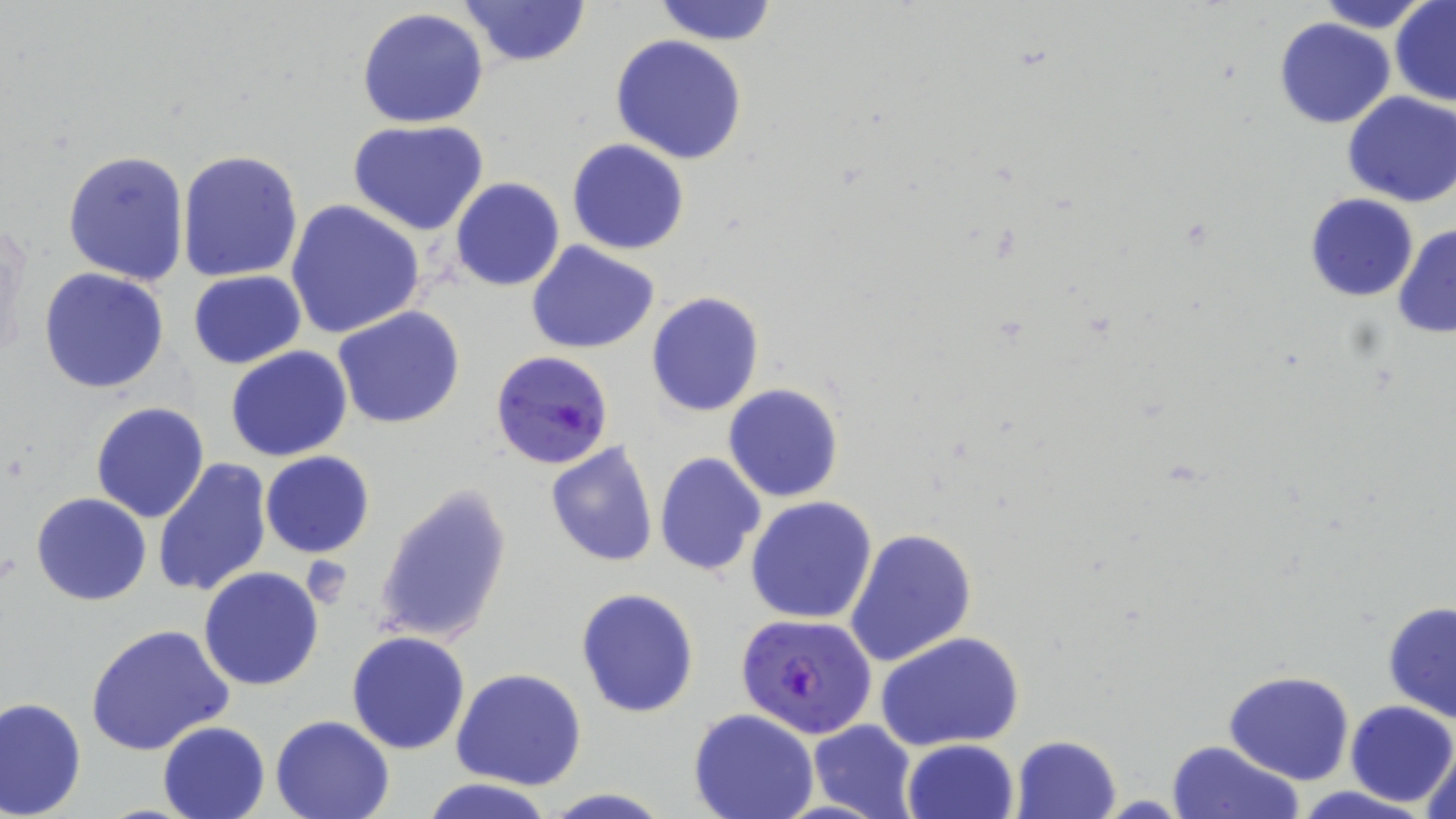
Summary:
  - Coordinate format: approximate bounding boxes as (x1,y1)-(x2,y2) corner pairs in pixels
  - Uninfected red blood cell locations: (456,0)-(593,68), (1322,0)-(1426,31), (653,1)-(780,46), (1390,1)-(1456,105), (355,8)-(489,129), (1274,17)-(1395,129), (611,35)-(747,165), (1342,92)-(1456,207), (347,120)-(489,236), (567,138)-(689,255), (62,148)-(191,287), (177,149)-(306,284), (450,178)-(564,291), (1304,193)-(1419,301), (284,200)-(426,340), (1392,222)-(1456,340), (526,242)-(659,352), (38,267)-(170,394), (189,271)-(306,368), (646,292)-(765,416), (332,306)-(465,429), (225,346)-(353,463), (723,385)-(843,503), (90,401)-(210,523), (544,441)-(661,568), (261,451)-(376,560), (654,453)-(766,576), (151,457)-(272,599), (372,485)-(513,648), (30,492)-(154,606), (746,496)-(878,625), (845,527)-(978,669), (199,567)-(325,691), (576,587)-(701,719), (1381,600)-(1456,725), (86,624)-(233,758), (346,630)-(471,754), (877,631)-(1025,751), (451,667)-(588,790), (1223,671)-(1354,786), (0,697)-(86,818), (1346,700)-(1456,807), (687,709)-(820,819), (270,714)-(396,819), (808,719)-(917,819), (157,720)-(271,819), (1011,734)-(1123,819), (901,738)-(1019,819), (1167,740)-(1303,819), (1422,741)-(1456,819), (420,777)-(555,819), (1283,787)-(1443,819), (542,788)-(675,819)
  - Plasmodium falciparum-infected red blood cell locations: (490,349)-(614,470), (735,613)-(878,739)
  - Slide-level diagnosis: Plasmodium falciparum
  - Field of view: one of a larger specimen
  - Magnification: 1000x
  - Modality: light microscopy
  - Stain: May-Grünwald-Giemsa
  - Preparation: thin blood smear
  - Image size: 1456×819 pixels